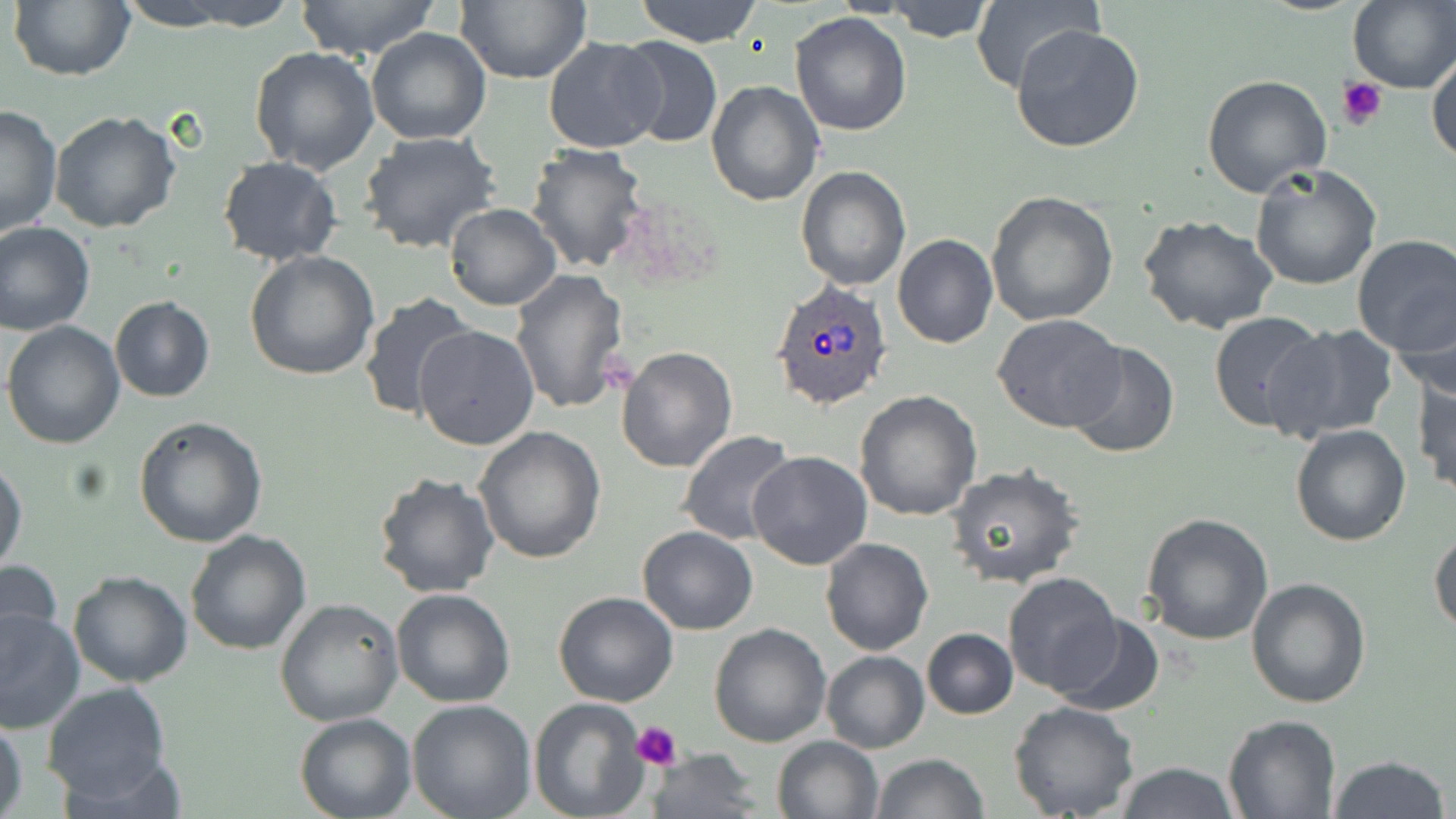
Summary:
  - Coordinate format: approximate bounding boxes as (x1, y1, x2, y2) in pixels
  - Platelet locations: (1336, 75, 1388, 130), (630, 719, 683, 768)
  - Plasmodium ovale-infected red blood cell locations: (771, 281, 893, 411)
  - Uninfected red blood cell locations: (8, 0, 134, 82), (113, 0, 252, 31), (166, 0, 301, 30), (295, 0, 442, 59), (456, 0, 591, 85), (635, 0, 764, 47), (885, 0, 995, 42), (970, 0, 1099, 95), (1348, 0, 1456, 92), (790, 10, 912, 136), (1010, 22, 1146, 154), (366, 28, 493, 147), (615, 36, 723, 149), (542, 38, 667, 153), (250, 45, 380, 175), (1428, 52, 1455, 168), (1203, 72, 1333, 197), (706, 79, 824, 206), (0, 102, 63, 240), (49, 110, 182, 232), (358, 130, 502, 256), (524, 144, 651, 273), (217, 156, 343, 266), (1249, 162, 1383, 290), (795, 166, 910, 291), (984, 191, 1118, 327), (444, 204, 560, 310), (1138, 216, 1280, 335), (0, 220, 96, 335), (1351, 233, 1456, 356), (893, 235, 998, 348), (245, 250, 380, 381), (510, 269, 631, 416), (358, 291, 477, 422), (1390, 294, 1456, 405), (109, 295, 215, 403), (1208, 310, 1328, 433), (992, 313, 1126, 433), (2, 321, 126, 449), (1267, 323, 1401, 442), (414, 324, 539, 451), (1065, 340, 1179, 460), (617, 346, 738, 473), (1413, 372, 1455, 496), (855, 390, 983, 521), (133, 416, 268, 548), (1290, 423, 1412, 547), (473, 425, 606, 564), (679, 431, 798, 545), (747, 452, 872, 571), (0, 457, 26, 575), (944, 466, 1086, 592), (372, 470, 500, 598), (1141, 514, 1274, 645), (636, 526, 759, 635), (1429, 527, 1456, 636), (185, 530, 312, 655), (821, 537, 933, 655), (0, 557, 64, 658), (68, 570, 192, 688), (1003, 572, 1124, 696), (1244, 575, 1370, 709), (391, 588, 516, 708), (552, 591, 680, 708), (274, 597, 403, 726), (0, 607, 84, 734), (1050, 611, 1164, 716), (709, 624, 831, 748), (921, 628, 1018, 719), (821, 650, 929, 753), (42, 682, 173, 803), (407, 699, 536, 819), (528, 699, 649, 819), (1009, 701, 1140, 819), (294, 713, 416, 819), (1223, 714, 1341, 817), (0, 716, 28, 818), (772, 735, 883, 819), (648, 748, 763, 818), (870, 753, 987, 819), (1329, 756, 1449, 819), (1115, 761, 1239, 819)
  - Slide-level diagnosis: Plasmodium ovale
  - Field of view: one of a larger specimen
  - Image size: 1456×819 pixels
  - Preparation: thin blood film
  - Magnification: 1000x
  - Stain: May-Grünwald-Giemsa
  - Modality: optical microscopy